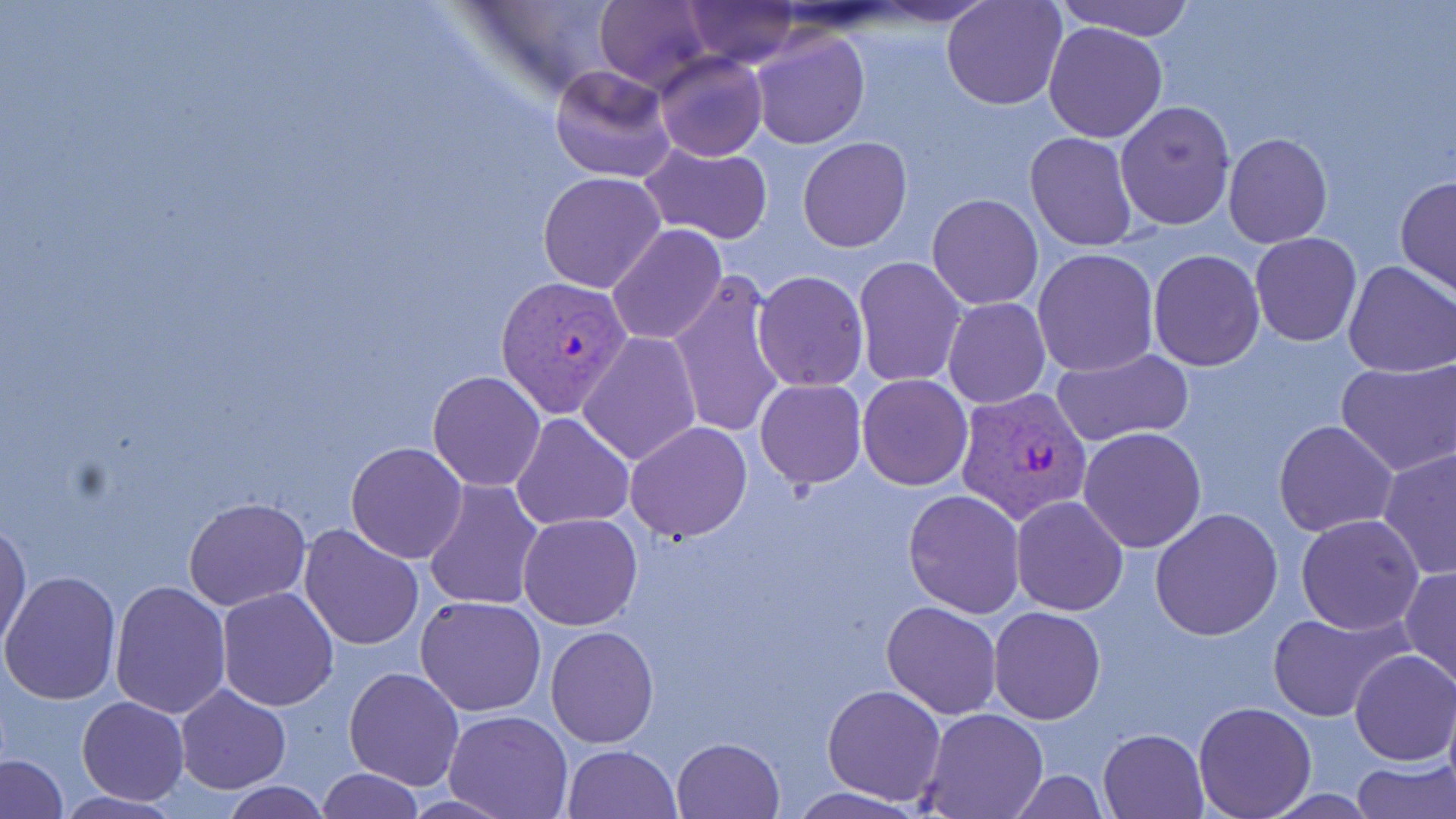
Approximate bounding boxes as (x1, y1, x2, y2) in pixels. Uninfected red blood cell locations: (596, 0, 711, 93), (684, 0, 799, 67), (942, 0, 1067, 110), (1051, 0, 1198, 39), (1043, 21, 1168, 143), (749, 29, 869, 150), (654, 52, 767, 162), (548, 64, 675, 183), (1115, 100, 1235, 231), (1025, 131, 1138, 250), (1223, 133, 1333, 248), (798, 137, 912, 251), (640, 140, 773, 243), (538, 170, 668, 293), (1395, 176, 1456, 297), (927, 193, 1043, 309), (606, 224, 728, 348), (1250, 232, 1361, 347), (1032, 248, 1159, 378), (1148, 249, 1264, 370), (853, 256, 967, 388), (1343, 260, 1456, 379), (667, 267, 788, 440), (753, 271, 867, 391), (944, 297, 1050, 408), (577, 331, 703, 466), (1049, 347, 1193, 448), (1335, 358, 1455, 477), (426, 371, 547, 492), (857, 375, 972, 491), (754, 378, 866, 488), (511, 412, 634, 530), (1273, 419, 1398, 536), (624, 422, 752, 543), (1078, 426, 1207, 553), (346, 442, 468, 564), (1378, 448, 1456, 578), (422, 477, 545, 612), (903, 490, 1025, 618), (1009, 495, 1129, 616), (184, 496, 310, 609), (1151, 509, 1281, 640), (516, 512, 642, 630), (1295, 513, 1423, 634), (0, 516, 31, 653), (297, 523, 425, 651), (1399, 565, 1456, 688), (2, 570, 121, 706), (109, 581, 232, 719), (216, 588, 339, 712), (415, 595, 547, 716), (881, 600, 1002, 719), (989, 606, 1106, 725), (1268, 609, 1407, 722), (546, 626, 660, 747), (1350, 649, 1456, 766), (343, 665, 466, 790), (821, 683, 947, 805), (174, 685, 292, 795), (77, 696, 188, 805), (1194, 700, 1317, 819), (917, 709, 1048, 819), (444, 710, 572, 819), (1098, 728, 1207, 819), (671, 737, 784, 819), (561, 744, 681, 819), (2, 754, 66, 819), (1351, 759, 1455, 819), (316, 767, 423, 818), (1006, 771, 1112, 817), (218, 781, 332, 818), (784, 787, 929, 819), (51, 790, 188, 819). Plasmodium vivax-infected red blood cell locations: (494, 275, 634, 419), (957, 384, 1094, 525). Slide-level diagnosis: Plasmodium vivax. 1000x magnification. Image is 1456×819 pixels. May-Grünwald-Giemsa stain. Light microscopy. Single field of view. Thin blood film.